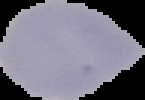

preparation: thin blood film
result: no Plasmodium parasites detected
image_size: 145×100 pixels
image_type: segmented cell region with the area outside set to black